Classify this cell by malaria status.
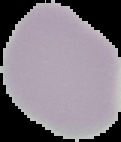

Uninfected.

Summary:
  - Preparation: thin blood film
  - Image size: 121×142 pixels
  - Image type: cell region segmented out of the field of view; surrounding area masked to black